Evaluate for Plasmodium parasites.
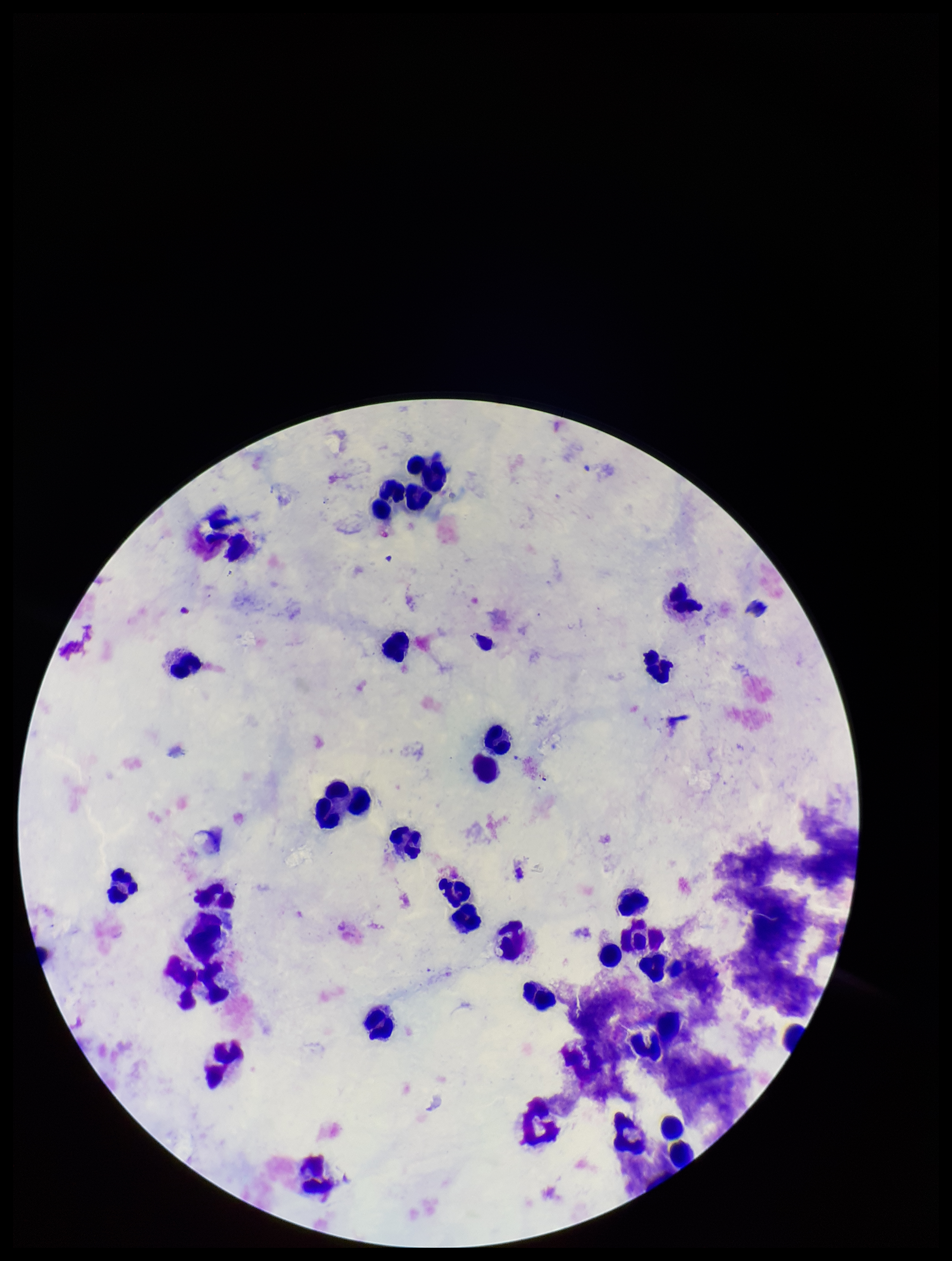

None identified.

Giemsa stain. Preparation: thick smear. Photographed through the microscope eyepiece with a smartphone camera. Patient malaria status: negative. Leukocyte count: 32. Parasite count: 0. Image is 952×1261 pixels. One field from this slide.